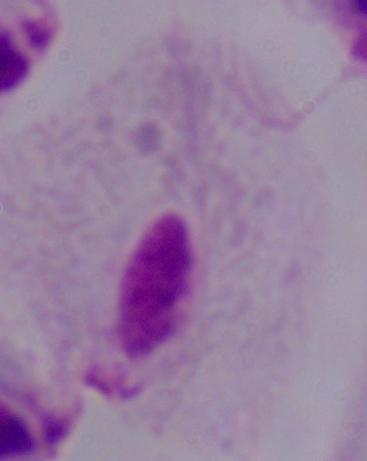

A trichomonad is seen. Photomicrograph. Captured at 1000x magnification.